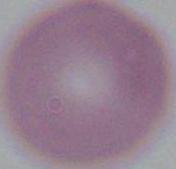
modality = photomicrograph
identification = red blood cell
magnification = 1000x